Classify this cell by malaria status.
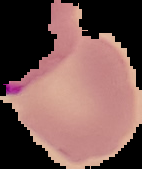
Uninfected.

Summary:
  - Image size: 142×169 pixels
  - Preparation: thin blood smear
  - Image type: segmented cell region on a black background